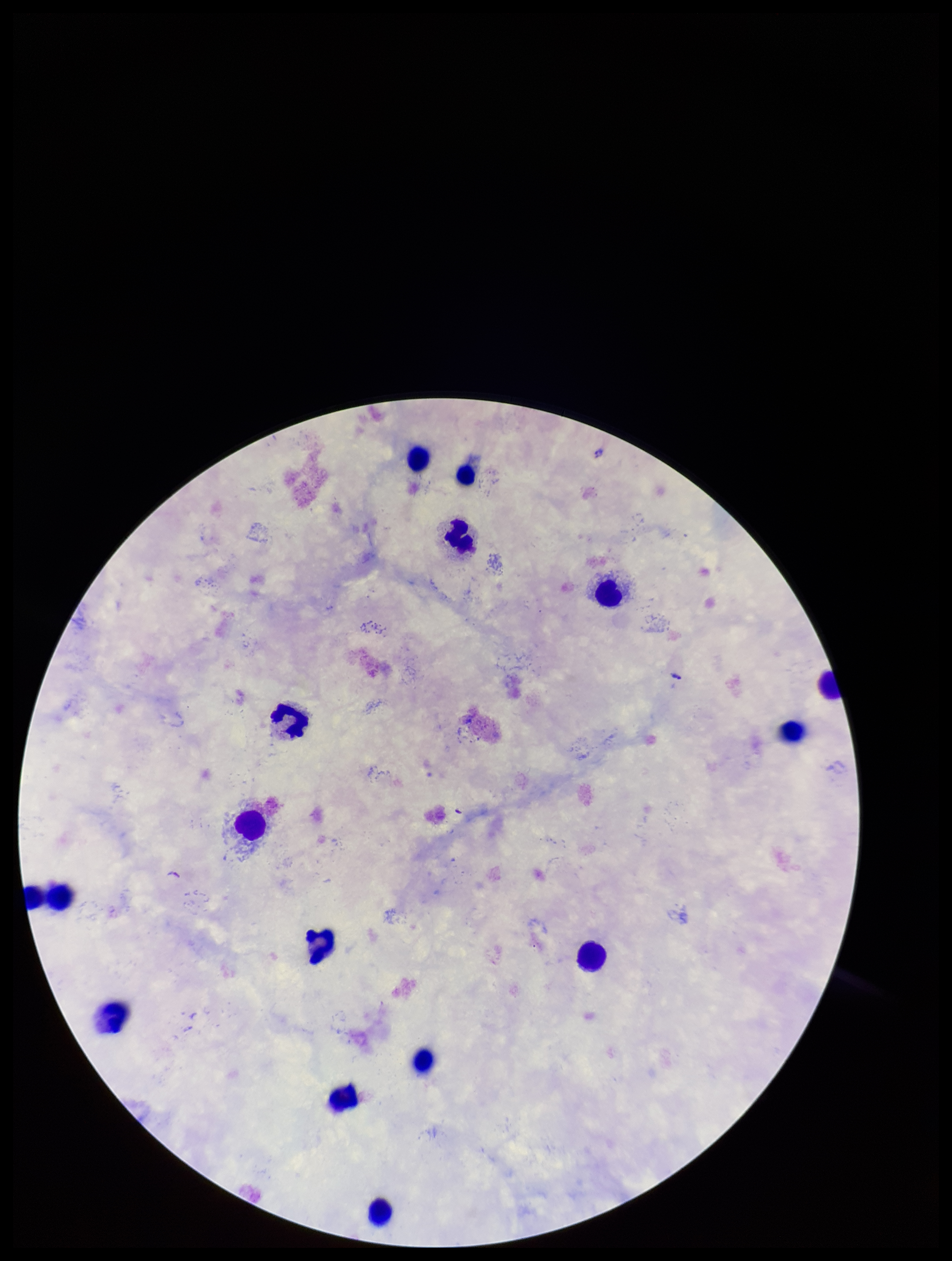
{
  "leukocyte_count": 16,
  "species_reported_for_this_patient": "Plasmodium falciparum",
  "patient_malaria_status": "positive",
  "image_size": "952×1261 pixels",
  "field_of_view": "one from this slide",
  "parasite_count": 0,
  "stain": "Giemsa",
  "preparation": "thick smear",
  "plasmodium_parasites": "none seen",
  "capture": "smartphone photograph through the microscope eyepiece"
}